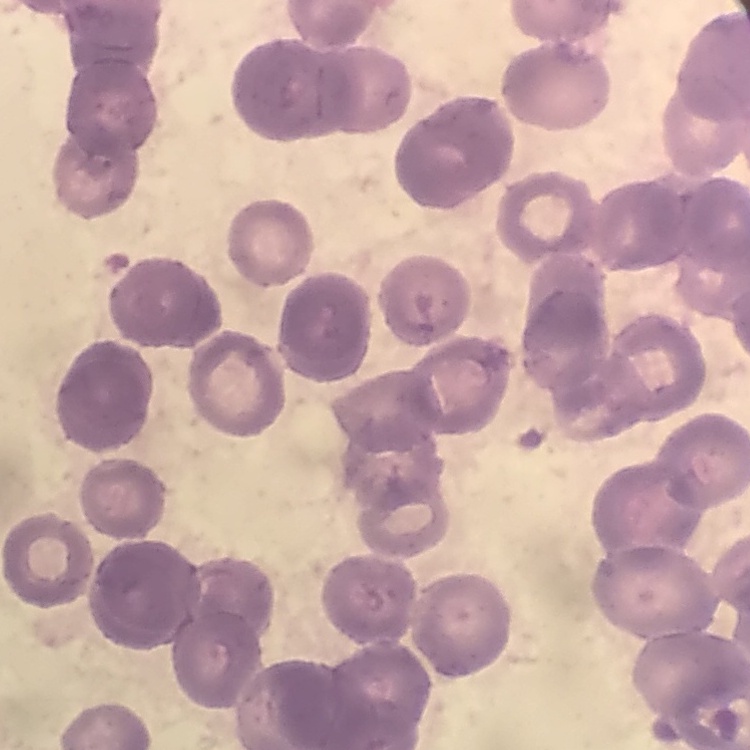

{
  "erythrocyte_morphology": "rouleaux formation",
  "stain": "Field's or Giemsa",
  "image_type": "one tile cut from a larger photomicrograph",
  "preparation": "thin blood film"
}